Name the parasite shown.
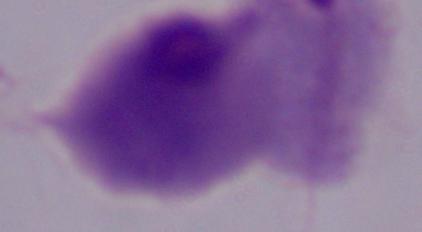
A trichomonad.

Summary:
  - Magnification: 1000x
  - Modality: photomicrograph